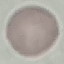
Summary:
  - Result: negative for malaria parasites
  - Stain: Giemsa
  - Capture: smartphone camera at the microscope eyepiece
  - Image type: cell patch, automatically extracted from a larger field of view and resized to 64 × 64 pixels
  - Preparation: thin blood film